Name the cell type shown.
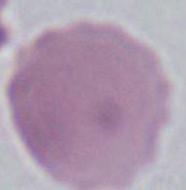
This is an erythrocyte.

modality = photomicrograph
magnification = 1000x